Give the position of every leukocyte visible.
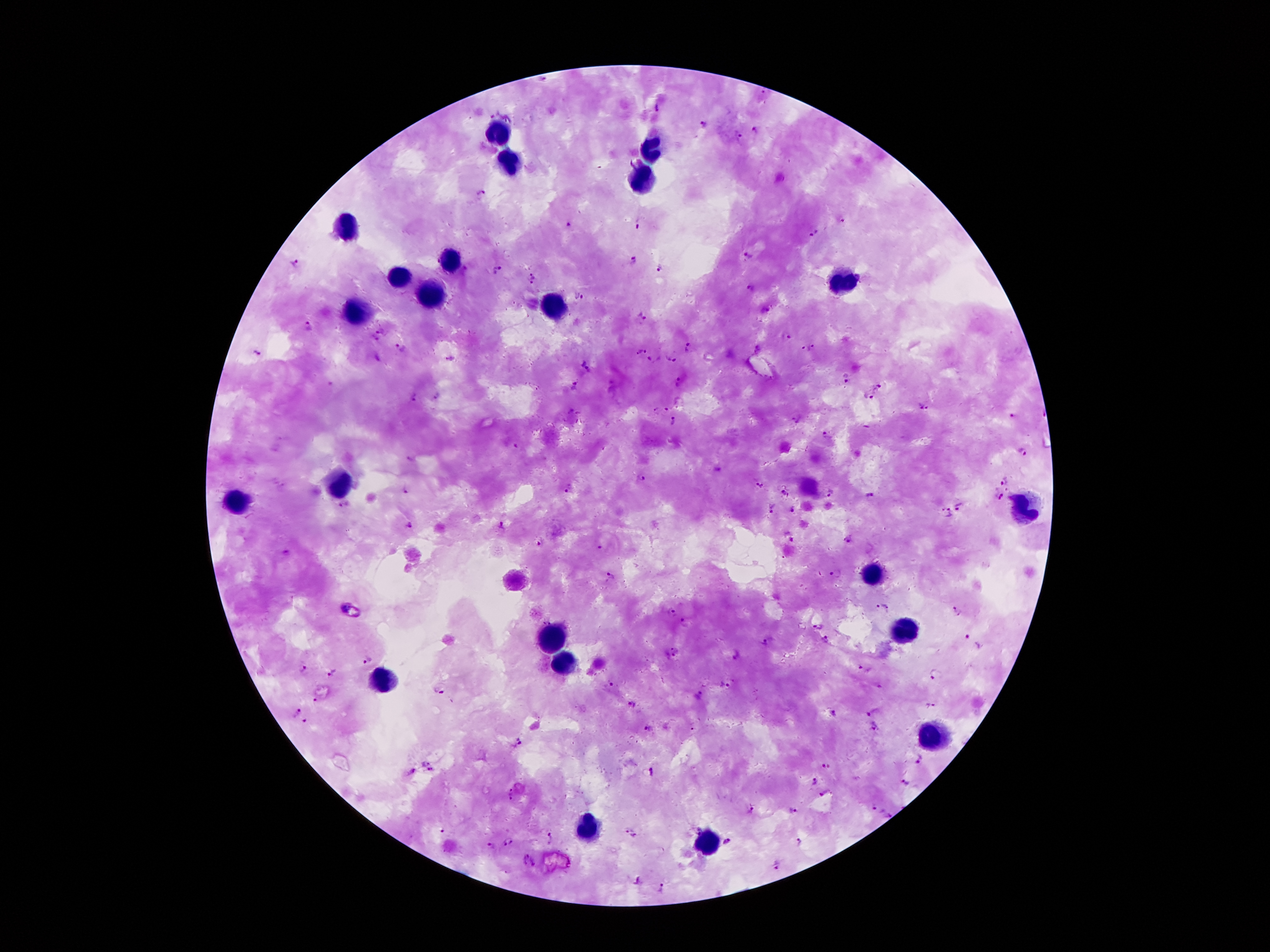

Approximate object centers, in pixels from the top-left corner.
Leukocytes: (x=504, y=139), (x=652, y=148), (x=511, y=164), (x=642, y=181), (x=348, y=227), (x=449, y=260), (x=395, y=276), (x=838, y=281), (x=428, y=295), (x=554, y=307), (x=351, y=316), (x=337, y=486), (x=238, y=500), (x=1025, y=507), (x=870, y=575), (x=901, y=629), (x=547, y=638), (x=563, y=663), (x=385, y=677), (x=931, y=736), (x=586, y=831), (x=707, y=843).

{
  "field_of_view": "one from this slide",
  "preparation": "thick blood smear",
  "capture": "smartphone camera through the microscope eyepiece",
  "magnification": "100x",
  "patient_malaria_status": "infected with Plasmodium falciparum",
  "stain": "Giemsa",
  "image_size": "1270×952 pixels",
  "plasmodium_parasite_locations": "approximate object centers, in pixels from the top-left corner: (x=543, y=79), (x=764, y=92), (x=658, y=108), (x=703, y=123), (x=756, y=131), (x=739, y=137), (x=481, y=192), (x=567, y=225), (x=636, y=225), (x=813, y=234), (x=750, y=257), (x=632, y=260), (x=294, y=263), (x=661, y=267), (x=496, y=271), (x=533, y=275), (x=528, y=283), (x=750, y=289), (x=580, y=297), (x=766, y=310), (x=643, y=315), (x=309, y=327), (x=379, y=330), (x=784, y=336), (x=374, y=338), (x=690, y=345), (x=809, y=348), (x=400, y=349), (x=257, y=351), (x=640, y=351), (x=449, y=358), (x=672, y=359), (x=653, y=360), (x=585, y=365), (x=847, y=375), (x=678, y=382), (x=574, y=385), (x=878, y=387), (x=414, y=397), (x=437, y=397), (x=870, y=397), (x=681, y=403), (x=924, y=407), (x=666, y=408), (x=656, y=409), (x=571, y=412), (x=1013, y=416), (x=795, y=419), (x=674, y=421), (x=825, y=435), (x=515, y=447), (x=1023, y=451), (x=640, y=477), (x=1005, y=479), (x=759, y=483), (x=569, y=487), (x=781, y=491), (x=831, y=492), (x=406, y=493), (x=872, y=493), (x=999, y=493), (x=344, y=505), (x=960, y=505), (x=773, y=509), (x=792, y=509), (x=947, y=512), (x=408, y=525), (x=500, y=526), (x=850, y=539), (x=540, y=543), (x=601, y=548), (x=837, y=574), (x=611, y=576), (x=885, y=607), (x=958, y=611), (x=672, y=614), (x=685, y=622), (x=820, y=627), (x=967, y=638), (x=826, y=640), (x=771, y=643), (x=674, y=653), (x=737, y=656), (x=368, y=660), (x=862, y=669), (x=304, y=670), (x=333, y=672), (x=935, y=674), (x=611, y=685), (x=727, y=685), (x=439, y=692), (x=699, y=696), (x=315, y=699), (x=632, y=704), (x=933, y=704), (x=873, y=712), (x=295, y=714), (x=834, y=714), (x=305, y=722), (x=648, y=730), (x=520, y=744), (x=426, y=760), (x=920, y=761), (x=828, y=765), (x=412, y=770), (x=652, y=770), (x=432, y=772), (x=816, y=780), (x=906, y=783), (x=824, y=792), (x=513, y=795), (x=872, y=806), (x=750, y=809), (x=794, y=809), (x=890, y=815), (x=442, y=830), (x=633, y=833), (x=551, y=839), (x=507, y=841), (x=798, y=842), (x=725, y=843), (x=489, y=847), (x=528, y=859), (x=778, y=863), (x=664, y=888)"
}